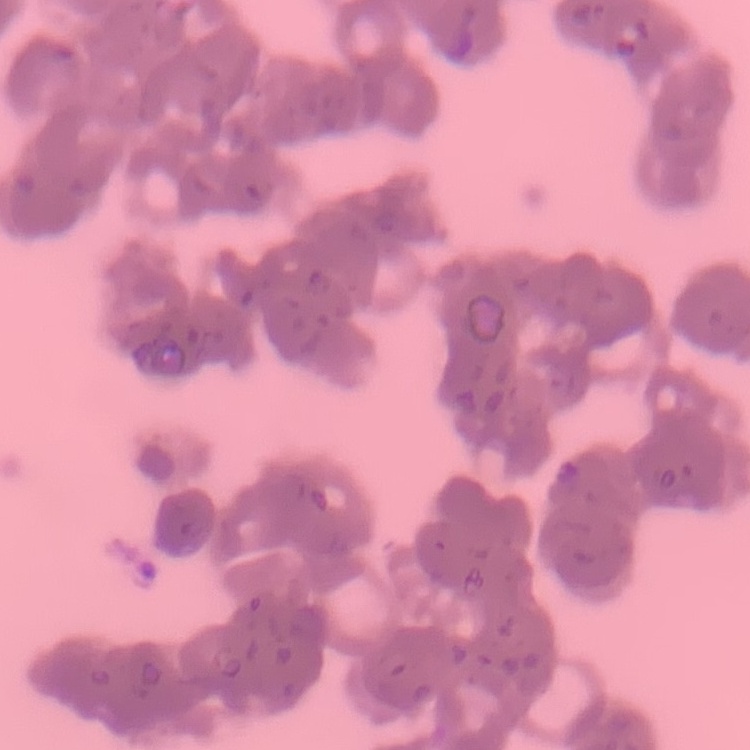
The red blood cells exhibit rouleaux formation. One tile cut from a larger photomicrograph. Thin blood film. Stained with either Field's or Giemsa.